State the blood parasite species.
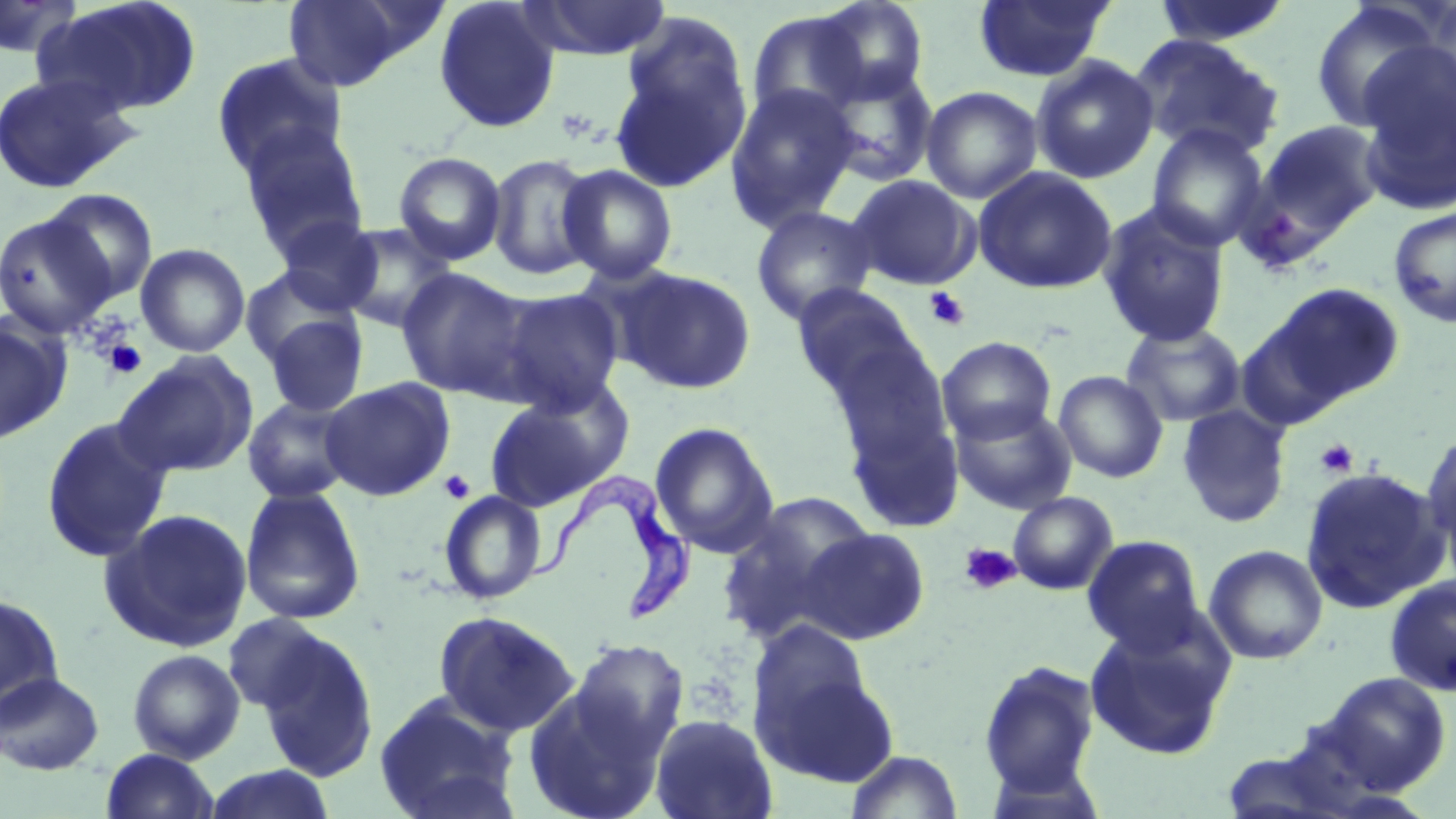

Trypanosoma brucei.

Approximate bounding boxes as [x1, y1, x2, y2] in pixels. Uninfected red blood cell locations: [0, 0, 83, 60], [38, 0, 202, 117], [280, 0, 434, 91], [433, 0, 561, 134], [519, 0, 671, 61], [973, 0, 1116, 83], [1151, 0, 1294, 47], [808, 1, 931, 105], [1310, 3, 1442, 133], [745, 9, 873, 125], [610, 18, 753, 193], [1129, 34, 1285, 160], [1355, 39, 1456, 211], [211, 52, 348, 179], [1031, 55, 1158, 184], [820, 64, 938, 186], [0, 72, 139, 194], [725, 83, 859, 231], [921, 86, 1042, 204], [1256, 120, 1386, 239], [237, 124, 369, 258], [1146, 124, 1270, 252], [393, 151, 506, 265], [486, 153, 600, 282], [557, 163, 679, 285], [973, 166, 1118, 294], [847, 175, 980, 290], [41, 189, 159, 305], [1097, 202, 1231, 348], [750, 205, 879, 326], [1388, 206, 1456, 328], [0, 212, 118, 339], [277, 217, 384, 315], [338, 223, 458, 332], [135, 243, 250, 358], [240, 267, 356, 369], [615, 267, 757, 395], [396, 268, 531, 399], [1264, 282, 1405, 407], [791, 283, 925, 402], [494, 288, 625, 413], [262, 311, 368, 417], [0, 315, 69, 444], [1121, 321, 1246, 427], [937, 336, 1056, 443], [823, 337, 953, 466], [112, 351, 259, 479], [1053, 370, 1168, 483], [319, 377, 455, 500], [483, 385, 626, 512], [242, 396, 357, 504], [949, 402, 1077, 514], [1177, 404, 1291, 528], [844, 409, 965, 533], [41, 416, 173, 563], [649, 422, 779, 557], [1421, 427, 1456, 565], [1298, 465, 1449, 614], [239, 486, 366, 625], [438, 490, 547, 605], [716, 492, 875, 644], [1007, 492, 1118, 595], [99, 507, 253, 652], [794, 527, 931, 645], [1082, 535, 1205, 653], [1204, 544, 1328, 665], [1384, 575, 1456, 696], [0, 592, 66, 719], [433, 610, 581, 737], [221, 613, 338, 717], [747, 618, 876, 740], [1083, 618, 1235, 761], [253, 628, 379, 782], [567, 639, 689, 763], [127, 649, 246, 763], [977, 659, 1101, 796], [759, 663, 900, 790], [0, 671, 105, 775], [1316, 671, 1452, 795], [521, 679, 667, 819], [373, 692, 521, 819], [649, 713, 778, 819], [100, 748, 220, 819], [846, 749, 963, 818], [200, 766, 336, 819]. Platelet locations: [923, 287, 970, 331], [103, 339, 147, 379], [1315, 438, 1359, 478], [438, 470, 475, 504], [959, 542, 1022, 595]. Trypanosoma brucei locations: [522, 472, 696, 625]. Thin blood smear. Single field of view. Image is 1456×819 pixels. Optical microscopy. May-Grünwald-Giemsa-stained preparation. 1000x magnification.